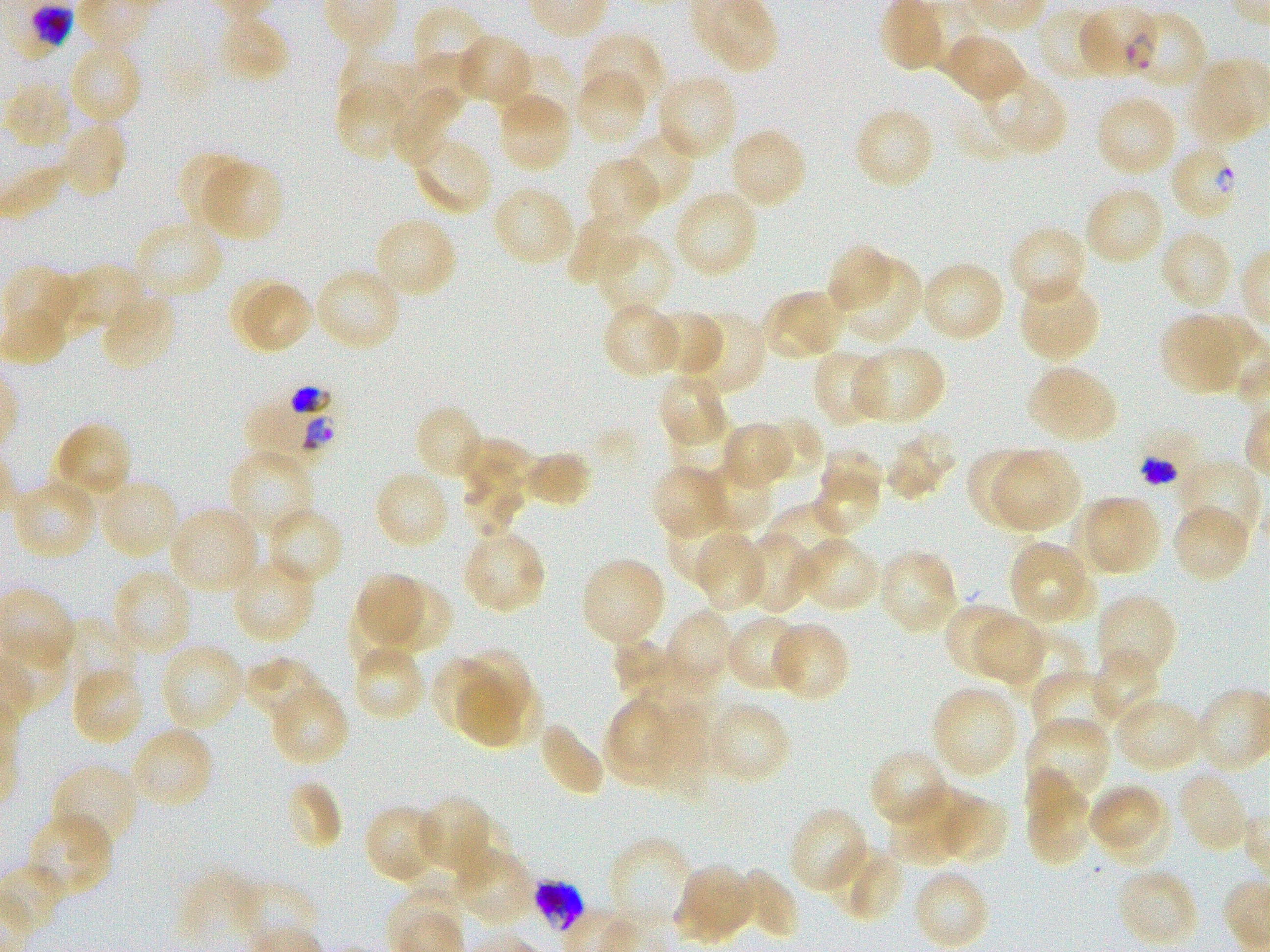

Not every red blood cell is marked. A life-cycle stage — or a range of stages, where the recorded stages span more than one — follows each staged infected red blood cell.
stain = Giemsa
locations of uninfected red blood cells = approximate bounding rectangles given as corner coordinates in pixels from the top-left: (x1=413, y1=7, x2=488, y2=80), (x1=1035, y1=8, x2=1111, y2=83), (x1=1156, y1=10, x2=1209, y2=88), (x1=218, y1=15, x2=291, y2=84), (x1=582, y1=33, x2=666, y2=112), (x1=942, y1=33, x2=1025, y2=104), (x1=455, y1=34, x2=534, y2=107), (x1=67, y1=42, x2=143, y2=126), (x1=335, y1=48, x2=415, y2=117), (x1=409, y1=52, x2=478, y2=113), (x1=506, y1=53, x2=579, y2=127), (x1=1187, y1=60, x2=1256, y2=144), (x1=981, y1=70, x2=1067, y2=156), (x1=574, y1=71, x2=646, y2=144), (x1=656, y1=73, x2=738, y2=161), (x1=3, y1=80, x2=72, y2=149), (x1=334, y1=81, x2=408, y2=161), (x1=391, y1=84, x2=461, y2=166), (x1=400, y1=85, x2=464, y2=127), (x1=495, y1=93, x2=572, y2=173), (x1=1095, y1=95, x2=1177, y2=177), (x1=853, y1=106, x2=936, y2=190), (x1=58, y1=121, x2=127, y2=200), (x1=729, y1=126, x2=807, y2=209), (x1=623, y1=129, x2=695, y2=209), (x1=412, y1=137, x2=493, y2=217), (x1=175, y1=149, x2=250, y2=226), (x1=586, y1=156, x2=660, y2=233), (x1=199, y1=159, x2=284, y2=242), (x1=1083, y1=185, x2=1164, y2=266), (x1=492, y1=186, x2=576, y2=267), (x1=674, y1=190, x2=760, y2=279), (x1=567, y1=213, x2=642, y2=287), (x1=371, y1=215, x2=458, y2=300), (x1=133, y1=218, x2=225, y2=301), (x1=1007, y1=224, x2=1088, y2=308), (x1=1159, y1=229, x2=1233, y2=311), (x1=593, y1=232, x2=673, y2=317), (x1=825, y1=243, x2=894, y2=317), (x1=839, y1=256, x2=922, y2=347), (x1=919, y1=260, x2=1007, y2=343), (x1=63, y1=265, x2=146, y2=337), (x1=314, y1=266, x2=403, y2=353), (x1=2, y1=267, x2=82, y2=337), (x1=1018, y1=278, x2=1102, y2=361), (x1=244, y1=285, x2=313, y2=351), (x1=760, y1=290, x2=843, y2=362), (x1=101, y1=295, x2=177, y2=372), (x1=601, y1=303, x2=682, y2=379), (x1=653, y1=309, x2=725, y2=378), (x1=685, y1=311, x2=766, y2=398), (x1=1158, y1=315, x2=1245, y2=395), (x1=851, y1=344, x2=947, y2=426), (x1=811, y1=349, x2=887, y2=428), (x1=1026, y1=365, x2=1118, y2=443), (x1=657, y1=372, x2=728, y2=447), (x1=414, y1=404, x2=486, y2=482), (x1=670, y1=414, x2=733, y2=476), (x1=759, y1=416, x2=823, y2=480), (x1=720, y1=420, x2=794, y2=488), (x1=51, y1=422, x2=134, y2=501), (x1=884, y1=429, x2=959, y2=500), (x1=454, y1=435, x2=536, y2=485), (x1=227, y1=447, x2=315, y2=536), (x1=964, y1=448, x2=1040, y2=530), (x1=820, y1=449, x2=882, y2=502), (x1=993, y1=449, x2=1080, y2=530), (x1=525, y1=450, x2=593, y2=509), (x1=1178, y1=459, x2=1262, y2=544), (x1=460, y1=460, x2=521, y2=536), (x1=701, y1=461, x2=773, y2=535), (x1=813, y1=462, x2=880, y2=534), (x1=650, y1=463, x2=727, y2=540), (x1=373, y1=470, x2=451, y2=549), (x1=9, y1=477, x2=98, y2=562), (x1=99, y1=477, x2=181, y2=560), (x1=1088, y1=496, x2=1160, y2=574), (x1=1071, y1=498, x2=1148, y2=574), (x1=1172, y1=503, x2=1251, y2=583), (x1=765, y1=505, x2=852, y2=571), (x1=267, y1=506, x2=345, y2=587), (x1=168, y1=507, x2=259, y2=595), (x1=666, y1=512, x2=744, y2=585), (x1=461, y1=529, x2=546, y2=614), (x1=741, y1=531, x2=815, y2=614), (x1=693, y1=533, x2=764, y2=611), (x1=797, y1=537, x2=880, y2=613), (x1=1008, y1=541, x2=1093, y2=626), (x1=877, y1=549, x2=959, y2=634), (x1=231, y1=556, x2=316, y2=643), (x1=580, y1=556, x2=666, y2=646), (x1=110, y1=568, x2=193, y2=657), (x1=356, y1=571, x2=425, y2=644), (x1=377, y1=577, x2=451, y2=653), (x1=1095, y1=593, x2=1178, y2=682), (x1=346, y1=598, x2=417, y2=674), (x1=942, y1=601, x2=1018, y2=677), (x1=664, y1=608, x2=734, y2=689), (x1=975, y1=614, x2=1049, y2=687), (x1=724, y1=615, x2=806, y2=692), (x1=63, y1=621, x2=138, y2=697), (x1=769, y1=621, x2=850, y2=702), (x1=1008, y1=629, x2=1089, y2=708), (x1=613, y1=637, x2=676, y2=702), (x1=159, y1=641, x2=245, y2=732), (x1=352, y1=644, x2=426, y2=720), (x1=462, y1=647, x2=533, y2=723), (x1=1092, y1=650, x2=1160, y2=727), (x1=244, y1=656, x2=326, y2=723), (x1=430, y1=656, x2=503, y2=738), (x1=70, y1=667, x2=145, y2=747), (x1=1032, y1=670, x2=1120, y2=746), (x1=456, y1=672, x2=521, y2=748), (x1=491, y1=680, x2=543, y2=745), (x1=269, y1=684, x2=349, y2=766), (x1=930, y1=684, x2=1018, y2=780), (x1=1114, y1=696, x2=1204, y2=773), (x1=604, y1=699, x2=680, y2=787), (x1=708, y1=700, x2=792, y2=785), (x1=650, y1=702, x2=712, y2=798), (x1=1026, y1=715, x2=1109, y2=807), (x1=539, y1=722, x2=607, y2=797), (x1=128, y1=725, x2=215, y2=810), (x1=869, y1=747, x2=951, y2=829), (x1=51, y1=763, x2=140, y2=851), (x1=1175, y1=770, x2=1249, y2=853), (x1=1025, y1=774, x2=1092, y2=867), (x1=284, y1=778, x2=344, y2=852), (x1=1087, y1=783, x2=1160, y2=847), (x1=892, y1=788, x2=974, y2=863), (x1=414, y1=795, x2=494, y2=877), (x1=936, y1=795, x2=1009, y2=864), (x1=364, y1=804, x2=444, y2=884), (x1=787, y1=806, x2=870, y2=894), (x1=26, y1=812, x2=114, y2=898), (x1=453, y1=812, x2=513, y2=886), (x1=608, y1=835, x2=693, y2=927), (x1=830, y1=845, x2=904, y2=923), (x1=454, y1=846, x2=535, y2=926), (x1=674, y1=864, x2=755, y2=944), (x1=1115, y1=866, x2=1200, y2=947), (x1=733, y1=868, x2=798, y2=940), (x1=912, y1=868, x2=991, y2=949), (x1=177, y1=869, x2=262, y2=947)
preparation = thin blood film
objective = 100x, oil immersion, numerical aperture 1.25
field of view = single
donor blood group = O+
image size = 1270×952 pixels
locations of infected red blood cells = approximate bounding rectangles given as corner coordinates in pixels from the top-left: (x1=1077, y1=6, x2=1157, y2=77) ring; (x1=1173, y1=149, x2=1234, y2=217) ring; (x1=243, y1=388, x2=335, y2=456); (x1=1137, y1=425, x2=1203, y2=489); (x1=530, y1=880, x2=584, y2=934) late trophozoite to early schizont
culture = static in-vitro Plasmodium falciparum strain 3D7